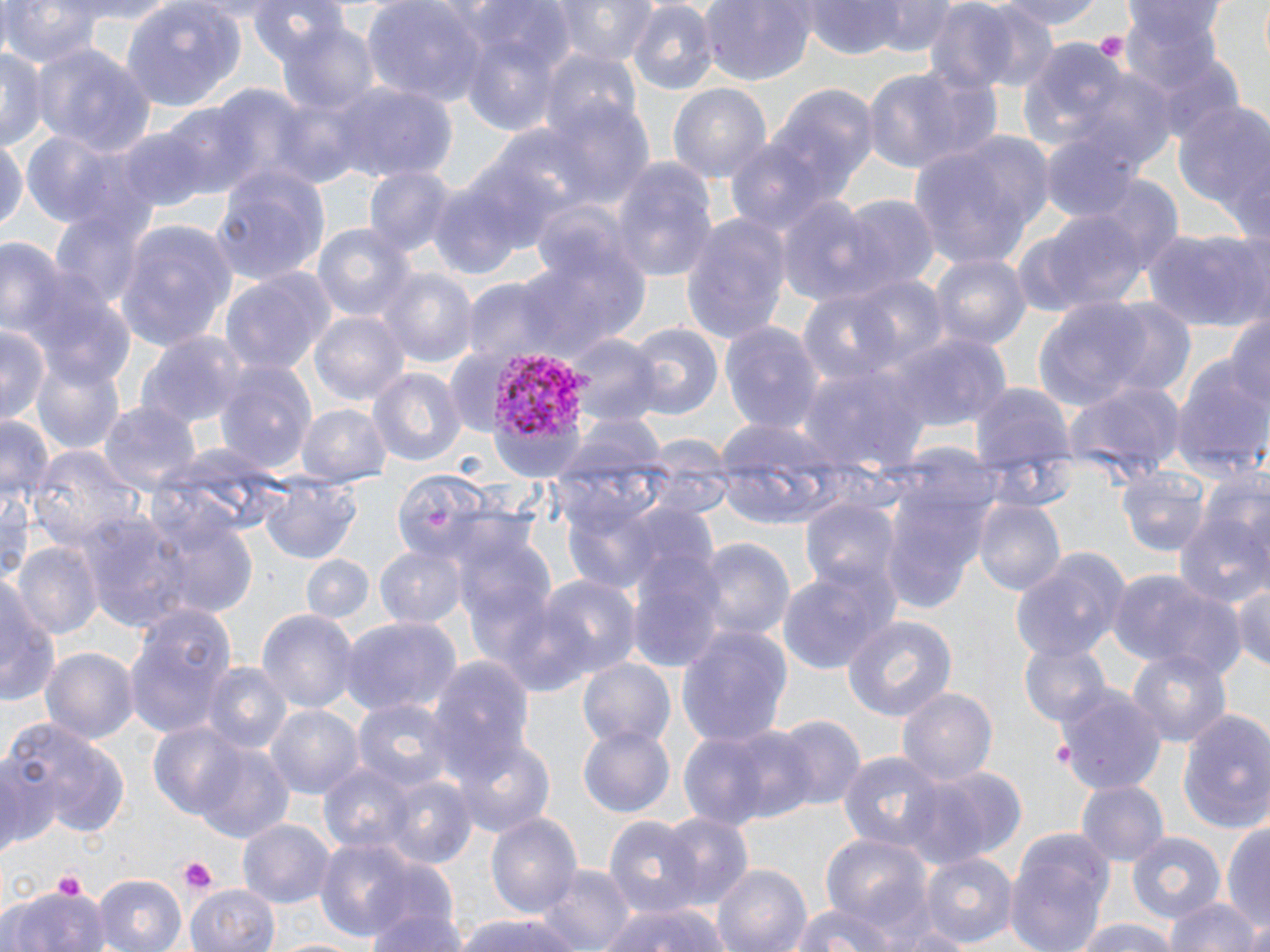 Approximate bounding boxes as named x1/y1/x2/y2 corners in pixels. Platelet locations: (x1=1099, y1=30, x2=1127, y2=59), (x1=177, y1=857, x2=220, y2=898), (x1=51, y1=869, x2=88, y2=898). Plasmodium vivax-infected red blood cell locations: (x1=486, y1=354, x2=588, y2=448). Uninfected red blood cell locations: (x1=0, y1=0, x2=102, y2=67), (x1=120, y1=0, x2=244, y2=109), (x1=245, y1=0, x2=355, y2=77), (x1=363, y1=0, x2=484, y2=106), (x1=546, y1=0, x2=656, y2=67), (x1=700, y1=0, x2=815, y2=88), (x1=873, y1=0, x2=955, y2=57), (x1=997, y1=0, x2=1105, y2=33), (x1=1119, y1=0, x2=1229, y2=92), (x1=802, y1=1, x2=906, y2=59), (x1=628, y1=2, x2=718, y2=95), (x1=924, y1=2, x2=1023, y2=96), (x1=962, y1=2, x2=1061, y2=95), (x1=450, y1=7, x2=577, y2=139), (x1=275, y1=20, x2=379, y2=119), (x1=1018, y1=35, x2=1127, y2=150), (x1=1, y1=41, x2=46, y2=151), (x1=31, y1=45, x2=153, y2=160), (x1=540, y1=50, x2=646, y2=146), (x1=859, y1=63, x2=986, y2=174), (x1=1070, y1=71, x2=1179, y2=175), (x1=765, y1=78, x2=877, y2=204), (x1=668, y1=83, x2=773, y2=188), (x1=210, y1=85, x2=313, y2=196), (x1=328, y1=85, x2=457, y2=186), (x1=1173, y1=95, x2=1268, y2=226), (x1=533, y1=97, x2=656, y2=213), (x1=158, y1=103, x2=254, y2=201), (x1=113, y1=127, x2=211, y2=210), (x1=22, y1=130, x2=127, y2=219), (x1=907, y1=130, x2=1051, y2=271), (x1=721, y1=132, x2=844, y2=242), (x1=0, y1=134, x2=27, y2=239), (x1=1041, y1=134, x2=1140, y2=223), (x1=609, y1=155, x2=719, y2=283), (x1=209, y1=167, x2=331, y2=287), (x1=362, y1=167, x2=454, y2=261), (x1=1088, y1=175, x2=1183, y2=275), (x1=425, y1=176, x2=540, y2=284), (x1=774, y1=196, x2=891, y2=310), (x1=831, y1=198, x2=941, y2=296), (x1=1030, y1=211, x2=1150, y2=318), (x1=678, y1=215, x2=791, y2=345), (x1=311, y1=222, x2=415, y2=325), (x1=115, y1=223, x2=237, y2=353), (x1=1142, y1=226, x2=1270, y2=331), (x1=0, y1=239, x2=60, y2=331), (x1=511, y1=242, x2=647, y2=359), (x1=926, y1=250, x2=1030, y2=351), (x1=17, y1=267, x2=135, y2=389), (x1=221, y1=268, x2=335, y2=376), (x1=379, y1=268, x2=475, y2=367), (x1=800, y1=273, x2=941, y2=384), (x1=459, y1=275, x2=573, y2=370), (x1=1033, y1=300, x2=1153, y2=417), (x1=1103, y1=300, x2=1198, y2=397), (x1=310, y1=312, x2=408, y2=409), (x1=1225, y1=312, x2=1270, y2=412), (x1=719, y1=319, x2=826, y2=432), (x1=624, y1=323, x2=722, y2=423), (x1=0, y1=324, x2=48, y2=428), (x1=140, y1=330, x2=247, y2=429), (x1=898, y1=332, x2=1014, y2=435), (x1=564, y1=333, x2=661, y2=427), (x1=31, y1=352, x2=128, y2=457), (x1=214, y1=358, x2=316, y2=475), (x1=1171, y1=361, x2=1270, y2=479), (x1=800, y1=366, x2=930, y2=475), (x1=370, y1=368, x2=465, y2=469), (x1=1063, y1=378, x2=1180, y2=489), (x1=968, y1=383, x2=1077, y2=490), (x1=100, y1=399, x2=201, y2=498), (x1=295, y1=404, x2=389, y2=489), (x1=0, y1=412, x2=54, y2=518), (x1=714, y1=417, x2=845, y2=534), (x1=639, y1=434, x2=736, y2=522), (x1=31, y1=444, x2=140, y2=551), (x1=1119, y1=462, x2=1214, y2=555), (x1=878, y1=471, x2=994, y2=614), (x1=259, y1=474, x2=361, y2=567), (x1=2, y1=480, x2=38, y2=586), (x1=1174, y1=483, x2=1268, y2=612), (x1=802, y1=499, x2=900, y2=600), (x1=975, y1=499, x2=1065, y2=598), (x1=145, y1=508, x2=261, y2=618), (x1=84, y1=517, x2=195, y2=634), (x1=692, y1=538, x2=794, y2=649), (x1=10, y1=541, x2=101, y2=640), (x1=376, y1=542, x2=467, y2=627), (x1=1013, y1=547, x2=1133, y2=663), (x1=624, y1=548, x2=729, y2=673), (x1=298, y1=555, x2=377, y2=627), (x1=776, y1=566, x2=891, y2=677), (x1=1106, y1=568, x2=1243, y2=677), (x1=0, y1=571, x2=60, y2=712), (x1=524, y1=574, x2=642, y2=684), (x1=1231, y1=577, x2=1270, y2=679), (x1=126, y1=604, x2=238, y2=740), (x1=258, y1=608, x2=358, y2=715), (x1=841, y1=613, x2=957, y2=721), (x1=339, y1=617, x2=462, y2=716), (x1=676, y1=626, x2=792, y2=748), (x1=1025, y1=645, x2=1113, y2=731), (x1=41, y1=646, x2=136, y2=746), (x1=1125, y1=647, x2=1232, y2=750), (x1=425, y1=656, x2=533, y2=785), (x1=578, y1=657, x2=675, y2=752), (x1=201, y1=663, x2=291, y2=758), (x1=1057, y1=685, x2=1167, y2=796), (x1=897, y1=686, x2=998, y2=791), (x1=355, y1=699, x2=453, y2=790), (x1=265, y1=702, x2=364, y2=801), (x1=1180, y1=708, x2=1270, y2=833), (x1=770, y1=716, x2=864, y2=811), (x1=5, y1=720, x2=130, y2=840), (x1=143, y1=720, x2=257, y2=824), (x1=681, y1=722, x2=817, y2=828), (x1=579, y1=726, x2=674, y2=816), (x1=449, y1=736, x2=560, y2=840), (x1=185, y1=743, x2=294, y2=840), (x1=838, y1=749, x2=947, y2=858), (x1=1, y1=752, x2=57, y2=858), (x1=318, y1=760, x2=421, y2=857), (x1=920, y1=767, x2=1029, y2=865), (x1=381, y1=776, x2=475, y2=870), (x1=1074, y1=779, x2=1169, y2=866), (x1=658, y1=809, x2=754, y2=909), (x1=486, y1=812, x2=584, y2=920), (x1=603, y1=814, x2=703, y2=919), (x1=238, y1=816, x2=336, y2=909), (x1=1224, y1=820, x2=1270, y2=933), (x1=1124, y1=829, x2=1224, y2=930), (x1=1004, y1=831, x2=1116, y2=952), (x1=822, y1=835, x2=932, y2=935), (x1=310, y1=839, x2=428, y2=939), (x1=921, y1=852, x2=1015, y2=949), (x1=536, y1=862, x2=635, y2=952), (x1=712, y1=862, x2=816, y2=952), (x1=358, y1=867, x2=467, y2=952), (x1=94, y1=874, x2=185, y2=951), (x1=185, y1=884, x2=282, y2=952), (x1=4, y1=887, x2=109, y2=952), (x1=1165, y1=896, x2=1262, y2=952), (x1=787, y1=900, x2=901, y2=952), (x1=594, y1=901, x2=736, y2=952), (x1=1241, y1=911, x2=1270, y2=952), (x1=458, y1=914, x2=580, y2=952), (x1=1071, y1=917, x2=1179, y2=952), (x1=884, y1=924, x2=976, y2=952), (x1=272, y1=935, x2=369, y2=952). Slide-level diagnosis: Plasmodium vivax. Thin blood smear. May-Grünwald-Giemsa stain. Image is 1270×952 pixels. Single field of view. 1000x magnification. Light microscopy.